Assess the morphology of the red blood cells.
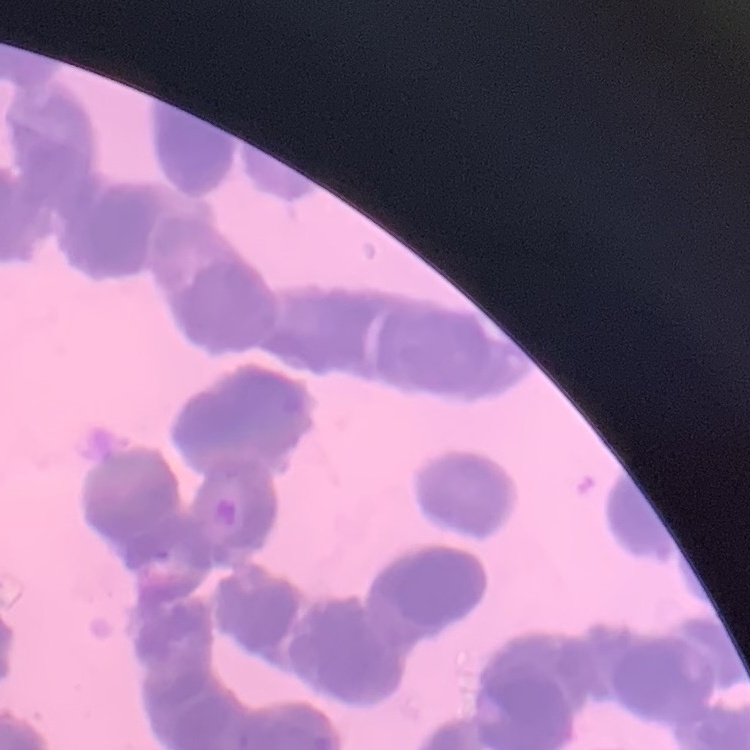

They show rouleaux formation.

preparation = thin blood film
image type = square crop of a larger photomicrograph
stain = Field's or Giemsa